Outline each blood parasite and name the species.
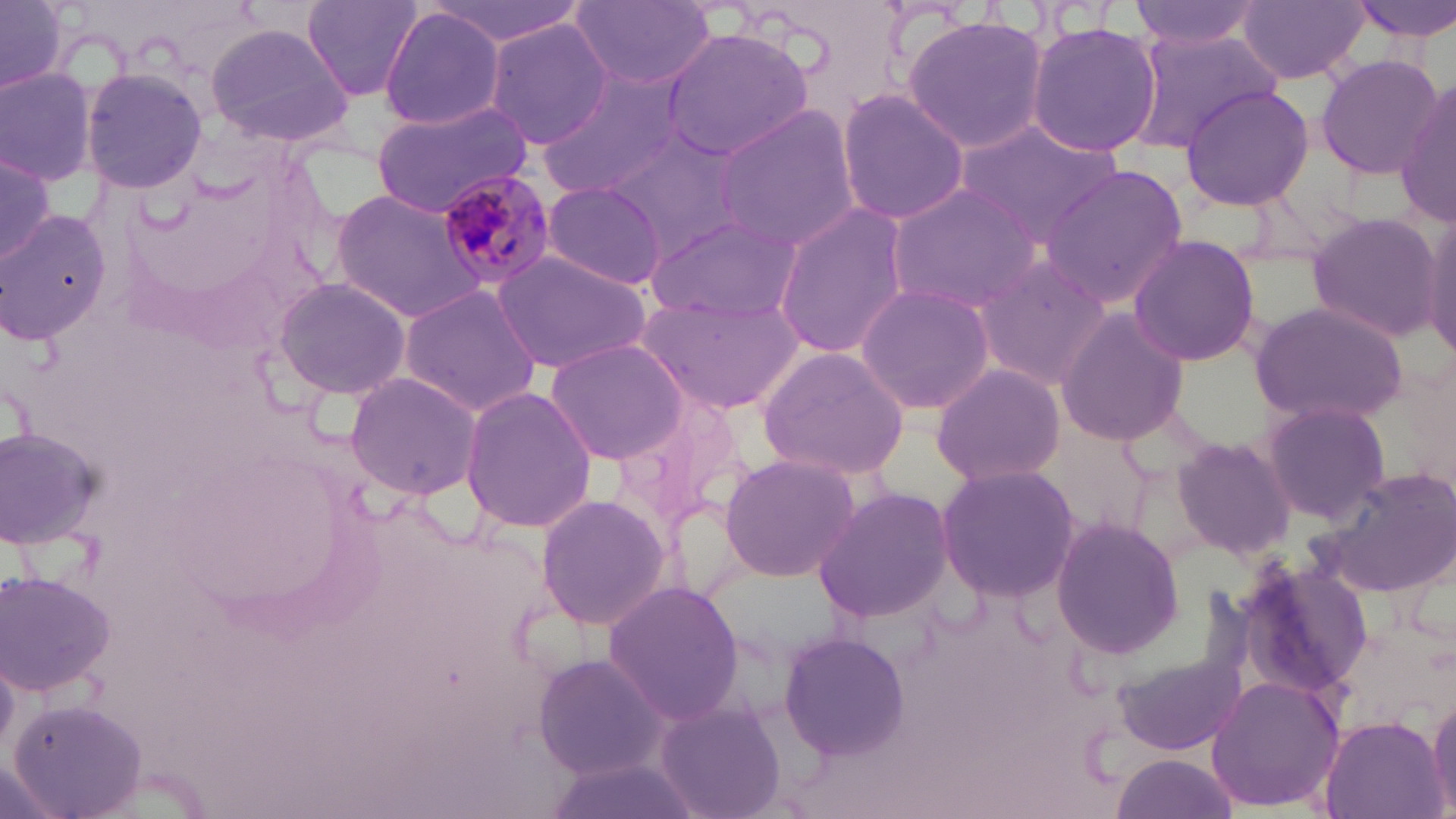
Approximate bounding boxes as named x1/y1/x2/y2 corners in pixels.
Plasmodium malariae-infected red blood cells: (x1=433, y1=168, x2=556, y2=293).
No Plasmodium falciparum, Plasmodium ovale, Plasmodium vivax, Babesia divergens, or Trypanosoma brucei observed.

Uninfected red blood cell locations: (x1=1, y1=0, x2=71, y2=95), (x1=302, y1=0, x2=425, y2=102), (x1=428, y1=0, x2=586, y2=46), (x1=1126, y1=0, x2=1267, y2=48), (x1=1343, y1=0, x2=1456, y2=42), (x1=570, y1=1, x2=718, y2=90), (x1=1236, y1=2, x2=1369, y2=85), (x1=378, y1=7, x2=508, y2=131), (x1=903, y1=14, x2=1047, y2=155), (x1=486, y1=18, x2=610, y2=151), (x1=1025, y1=20, x2=1164, y2=157), (x1=205, y1=22, x2=355, y2=149), (x1=659, y1=26, x2=816, y2=161), (x1=1131, y1=30, x2=1280, y2=148), (x1=1313, y1=53, x2=1443, y2=178), (x1=0, y1=65, x2=99, y2=188), (x1=81, y1=67, x2=209, y2=195), (x1=535, y1=69, x2=687, y2=201), (x1=1395, y1=79, x2=1456, y2=226), (x1=1179, y1=86, x2=1315, y2=210), (x1=836, y1=87, x2=968, y2=228), (x1=371, y1=101, x2=535, y2=213), (x1=713, y1=104, x2=861, y2=252), (x1=954, y1=119, x2=1127, y2=245), (x1=605, y1=132, x2=745, y2=257), (x1=0, y1=148, x2=60, y2=271), (x1=1041, y1=164, x2=1188, y2=308), (x1=541, y1=181, x2=667, y2=289), (x1=886, y1=181, x2=1044, y2=312), (x1=331, y1=187, x2=490, y2=320), (x1=773, y1=202, x2=911, y2=360), (x1=1418, y1=206, x2=1456, y2=359), (x1=0, y1=209, x2=110, y2=349), (x1=1305, y1=210, x2=1443, y2=342), (x1=646, y1=214, x2=797, y2=322), (x1=1126, y1=234, x2=1261, y2=366), (x1=491, y1=250, x2=652, y2=376), (x1=973, y1=253, x2=1113, y2=391), (x1=271, y1=276, x2=413, y2=400), (x1=854, y1=283, x2=995, y2=414), (x1=399, y1=284, x2=543, y2=419), (x1=638, y1=290, x2=803, y2=415), (x1=1250, y1=301, x2=1409, y2=426), (x1=1054, y1=308, x2=1191, y2=447), (x1=546, y1=337, x2=690, y2=463), (x1=759, y1=344, x2=911, y2=482), (x1=929, y1=362, x2=1063, y2=488), (x1=343, y1=371, x2=485, y2=501), (x1=460, y1=385, x2=597, y2=534), (x1=614, y1=392, x2=747, y2=526), (x1=1260, y1=400, x2=1391, y2=527), (x1=0, y1=424, x2=103, y2=547), (x1=1171, y1=435, x2=1297, y2=559), (x1=718, y1=452, x2=861, y2=581), (x1=935, y1=464, x2=1079, y2=601), (x1=1317, y1=464, x2=1456, y2=598), (x1=810, y1=486, x2=957, y2=624), (x1=533, y1=493, x2=672, y2=632), (x1=1051, y1=518, x2=1183, y2=659), (x1=1234, y1=553, x2=1374, y2=700), (x1=2, y1=569, x2=118, y2=699), (x1=601, y1=581, x2=743, y2=726), (x1=779, y1=630, x2=911, y2=762), (x1=1114, y1=652, x2=1246, y2=756), (x1=532, y1=653, x2=670, y2=780), (x1=1206, y1=673, x2=1345, y2=812), (x1=1426, y1=687, x2=1456, y2=816), (x1=654, y1=698, x2=786, y2=819), (x1=10, y1=699, x2=150, y2=819), (x1=1318, y1=717, x2=1447, y2=819), (x1=1111, y1=754, x2=1239, y2=819). Slide-level diagnosis: Plasmodium malariae. May-Grünwald-Giemsa-stained preparation. Single field of view. Image is 1456×819 pixels. 1000x magnification. Thin blood smear. Optical microscopy.